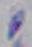
Summary:
  - Identification: Toxoplasma gondii
  - Modality: micrograph
  - Magnification: 1000x